Locate every blood parasite and identify its species.
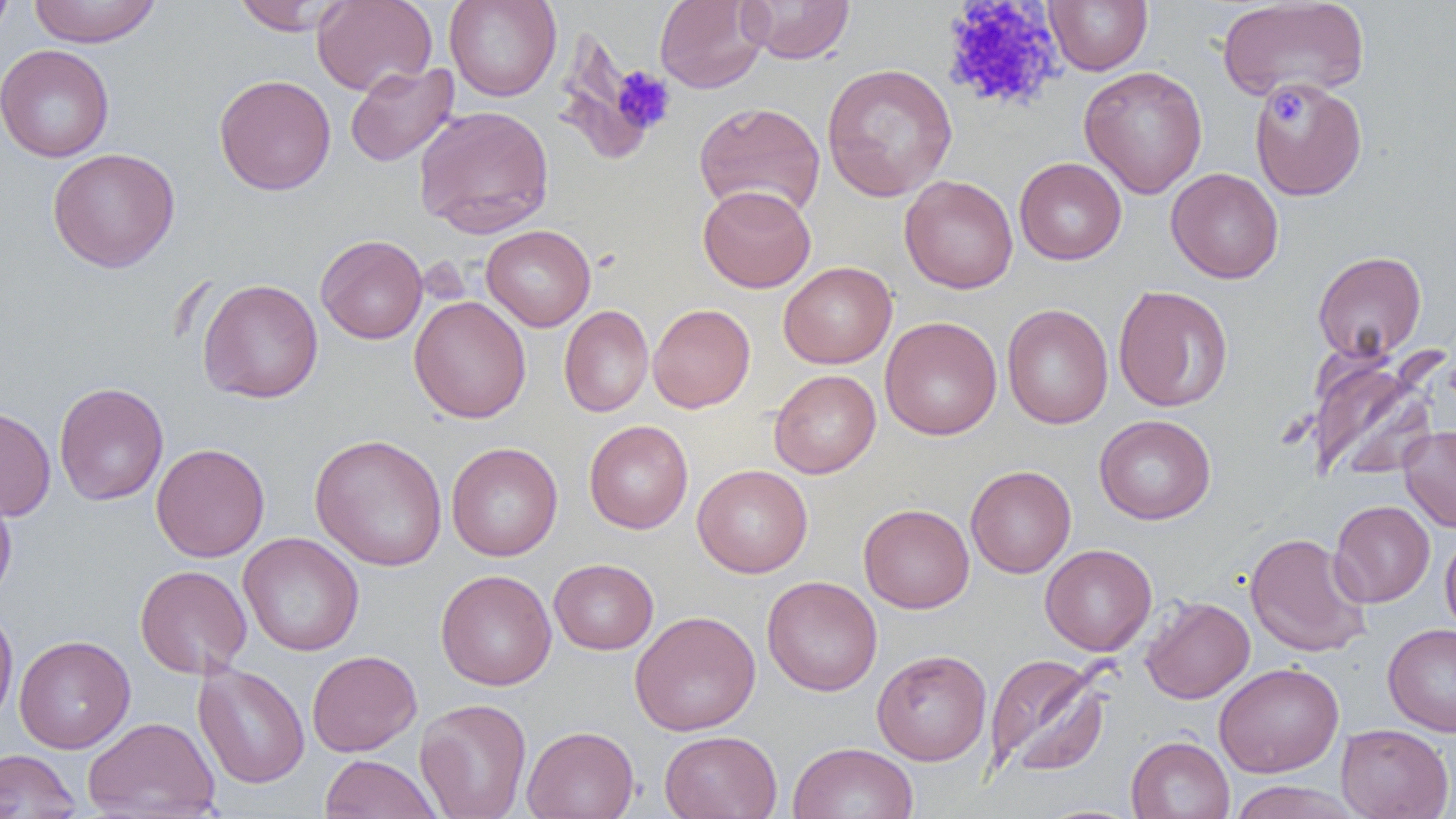

No blood parasites observed.

Approximate bounding boxes as [x1, y1, x2, y2] in pixels. Platelet locations: [940, 1, 1065, 114], [610, 66, 676, 134], [1270, 89, 1308, 126]. Uninfected red blood cell locations: [0, 0, 14, 46], [27, 0, 162, 47], [312, 0, 437, 96], [444, 0, 562, 102], [654, 0, 768, 94], [740, 0, 855, 64], [1044, 0, 1153, 75], [1216, 0, 1370, 101], [232, 1, 349, 35], [559, 26, 658, 164], [0, 44, 114, 162], [821, 62, 958, 201], [345, 63, 458, 167], [1079, 65, 1208, 199], [213, 74, 336, 196], [1250, 77, 1367, 201], [694, 101, 826, 220], [413, 105, 555, 237], [47, 147, 180, 273], [1014, 157, 1126, 265], [1166, 168, 1283, 284], [899, 175, 1018, 294], [698, 184, 816, 293], [481, 224, 596, 331], [315, 234, 428, 344], [1312, 251, 1427, 361], [779, 262, 897, 369], [197, 278, 323, 403], [1113, 285, 1233, 412], [409, 296, 531, 423], [648, 303, 755, 413], [1002, 304, 1113, 429], [559, 305, 653, 418], [880, 316, 1002, 440], [1308, 351, 1441, 482], [769, 369, 881, 478], [54, 382, 169, 506], [0, 405, 56, 521], [1094, 414, 1216, 524], [584, 420, 693, 534], [1399, 426, 1456, 532], [309, 433, 448, 572], [150, 442, 270, 562], [446, 442, 563, 561], [692, 464, 813, 578], [965, 465, 1076, 578], [0, 480, 17, 605], [1329, 500, 1435, 606], [859, 503, 975, 614], [1440, 529, 1456, 638], [238, 532, 364, 656], [1244, 532, 1371, 657], [1040, 544, 1157, 656], [549, 558, 659, 654], [135, 564, 252, 678], [435, 569, 556, 690], [762, 575, 882, 696], [1141, 596, 1255, 703], [0, 604, 18, 729], [629, 610, 761, 736], [1382, 623, 1456, 737], [14, 634, 135, 753], [872, 649, 992, 765], [306, 650, 422, 756], [984, 654, 1110, 777], [193, 661, 310, 789], [1214, 662, 1343, 778], [415, 698, 532, 819], [83, 716, 220, 818], [1336, 723, 1453, 819], [522, 725, 639, 819], [659, 730, 782, 819], [1126, 735, 1235, 819], [788, 741, 919, 819], [0, 749, 80, 819], [319, 754, 441, 818], [1227, 781, 1362, 819], [1032, 803, 1147, 819]. Slide-level diagnosis: no evidence of blood parasites. One field of a larger specimen. Captured at 1000x magnification. Image is 1456×819 pixels. Thin blood smear. Light microscopy.